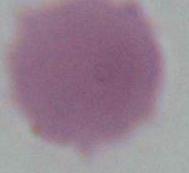 An erythrocyte is shown. Captured at 1000x magnification. Micrograph.